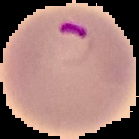

Result: malaria parasites identified. Cell region segmented out of the field of view; the surrounding area is masked to black. From a thin blood smear. Image is 139×139 pixels.